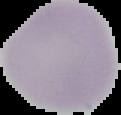
Summary:
  - Image size: 121×115 pixels
  - Image type: segmented cell region on a black background
  - Preparation: thin blood film
  - Malaria status: uninfected